Identify the parasite.
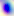
Toxoplasma gondii.

{
  "modality": "photomicrograph",
  "magnification": "400x"
}